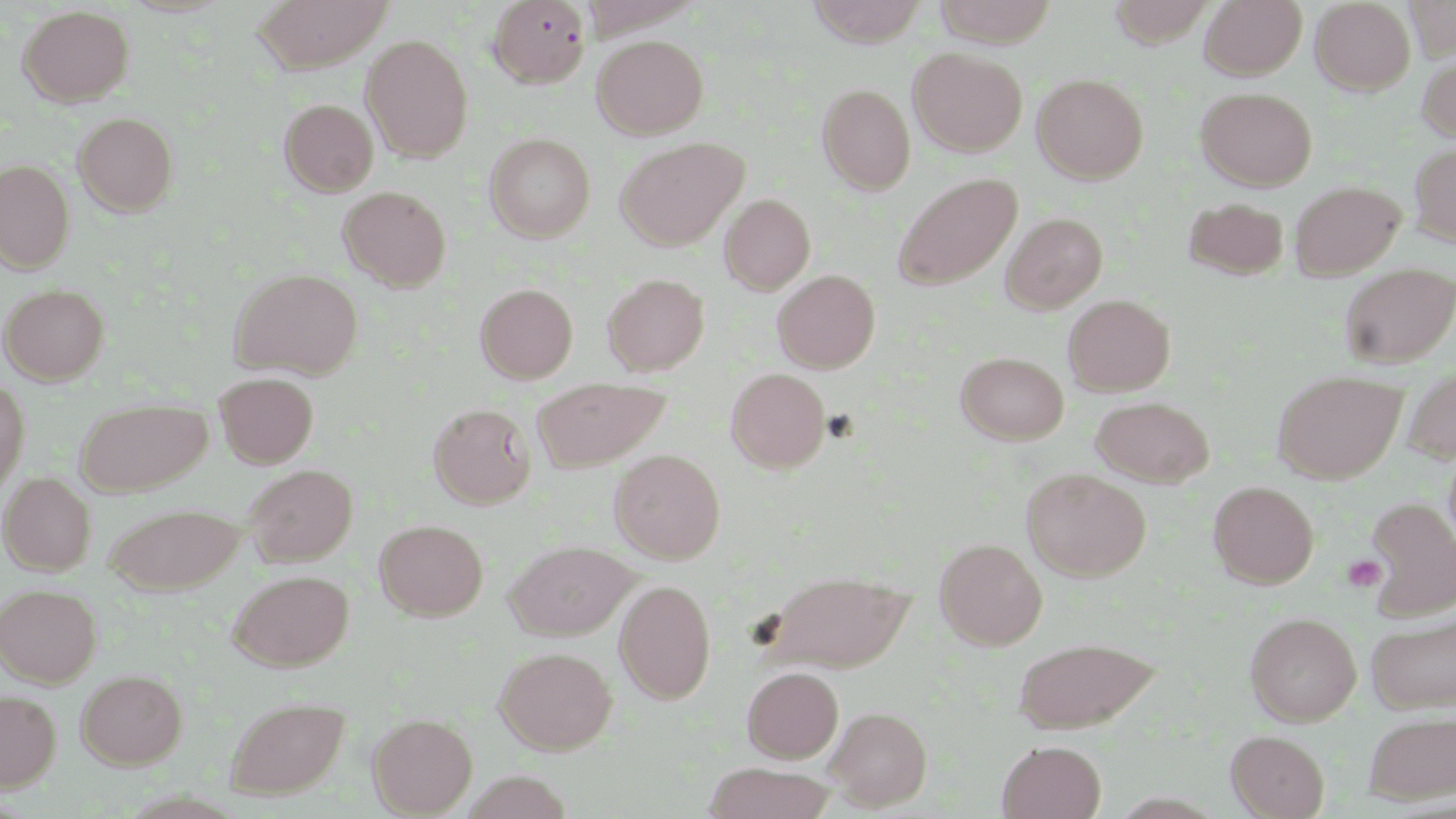

Summary:
  - Coordinate format: approximate bounding boxes as (x1, y1, x2, y2) in pixels
  - Uninfected red blood cell locations: (253, 0, 393, 71), (488, 0, 591, 88), (806, 0, 929, 46), (933, 0, 1058, 46), (1200, 0, 1307, 80), (1311, 0, 1415, 95), (1405, 0, 1455, 59), (1109, 1, 1217, 48), (17, 5, 134, 107), (361, 35, 473, 161), (592, 35, 708, 139), (908, 47, 1027, 157), (1417, 54, 1456, 143), (1032, 73, 1149, 183), (816, 83, 916, 194), (1196, 87, 1317, 191), (279, 98, 378, 196), (73, 112, 178, 216), (484, 133, 595, 242), (615, 136, 749, 250), (1409, 143, 1456, 246), (0, 160, 75, 272), (891, 173, 1023, 291), (1289, 181, 1405, 280), (338, 185, 451, 290), (720, 193, 815, 294), (1182, 196, 1290, 280), (1000, 212, 1108, 313), (1338, 263, 1455, 368), (229, 268, 363, 379), (773, 269, 880, 373), (602, 273, 710, 376), (1, 283, 109, 384), (475, 283, 578, 383), (1063, 293, 1175, 396), (956, 351, 1069, 444), (1402, 366, 1456, 464), (726, 368, 830, 472), (1273, 370, 1405, 484), (215, 372, 319, 467), (0, 376, 30, 493), (533, 379, 670, 472), (1090, 395, 1215, 487), (75, 399, 211, 496), (429, 402, 536, 509), (610, 448, 725, 563), (244, 463, 357, 566), (1022, 468, 1151, 581), (1, 472, 95, 575), (1208, 480, 1319, 588), (1364, 496, 1456, 622), (105, 502, 246, 594), (374, 519, 488, 620), (935, 538, 1048, 650), (507, 539, 636, 640), (228, 569, 354, 670), (765, 570, 915, 672), (615, 579, 716, 703), (0, 583, 102, 687), (1367, 611, 1456, 715), (1245, 612, 1361, 726), (1012, 636, 1160, 732), (495, 645, 617, 754), (742, 666, 843, 762), (76, 669, 187, 769), (0, 690, 61, 791), (225, 695, 350, 800), (826, 706, 932, 811), (1363, 709, 1456, 804), (368, 713, 477, 816), (1226, 730, 1329, 818), (997, 740, 1106, 819), (702, 763, 837, 819)
  - Platelet locations: (1343, 556, 1386, 593)
  - Slide-level diagnosis: negative for blood parasites
  - Image size: 1456×819 pixels
  - Field of view: single
  - Magnification: 1000x
  - Stain: May-Grünwald-Giemsa
  - Modality: light microscopy
  - Preparation: thin blood smear